Report the malaria status of this cell.
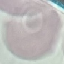

Uninfected.

capture = smartphone camera at the microscope eyepiece
image type = automatically extracted cell patch, resized to 64 × 64 pixels
stain = Giemsa
preparation = thin blood smear